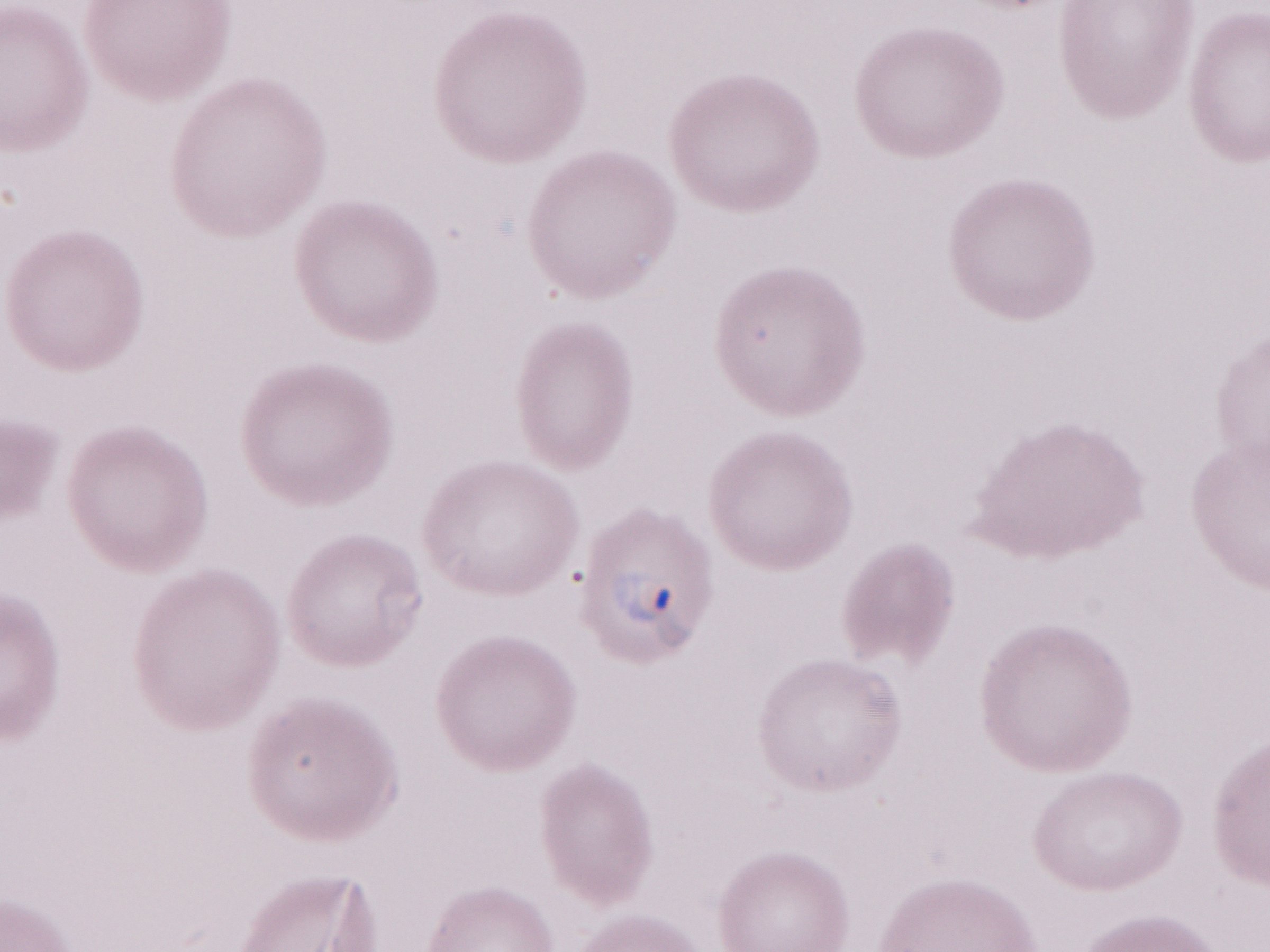 May-Grünwald-Giemsa-stained preparation. One field of this slide. Olympus BX43 microscope and DP73 digital camera. 1,000x magnification. Image is 1270×952 pixels. Thin blood smear. Patient diagnosis: malaria infection.